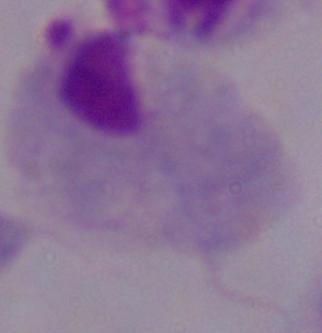

A trichomonad is seen. Captured at 1000x magnification. Photomicrograph.